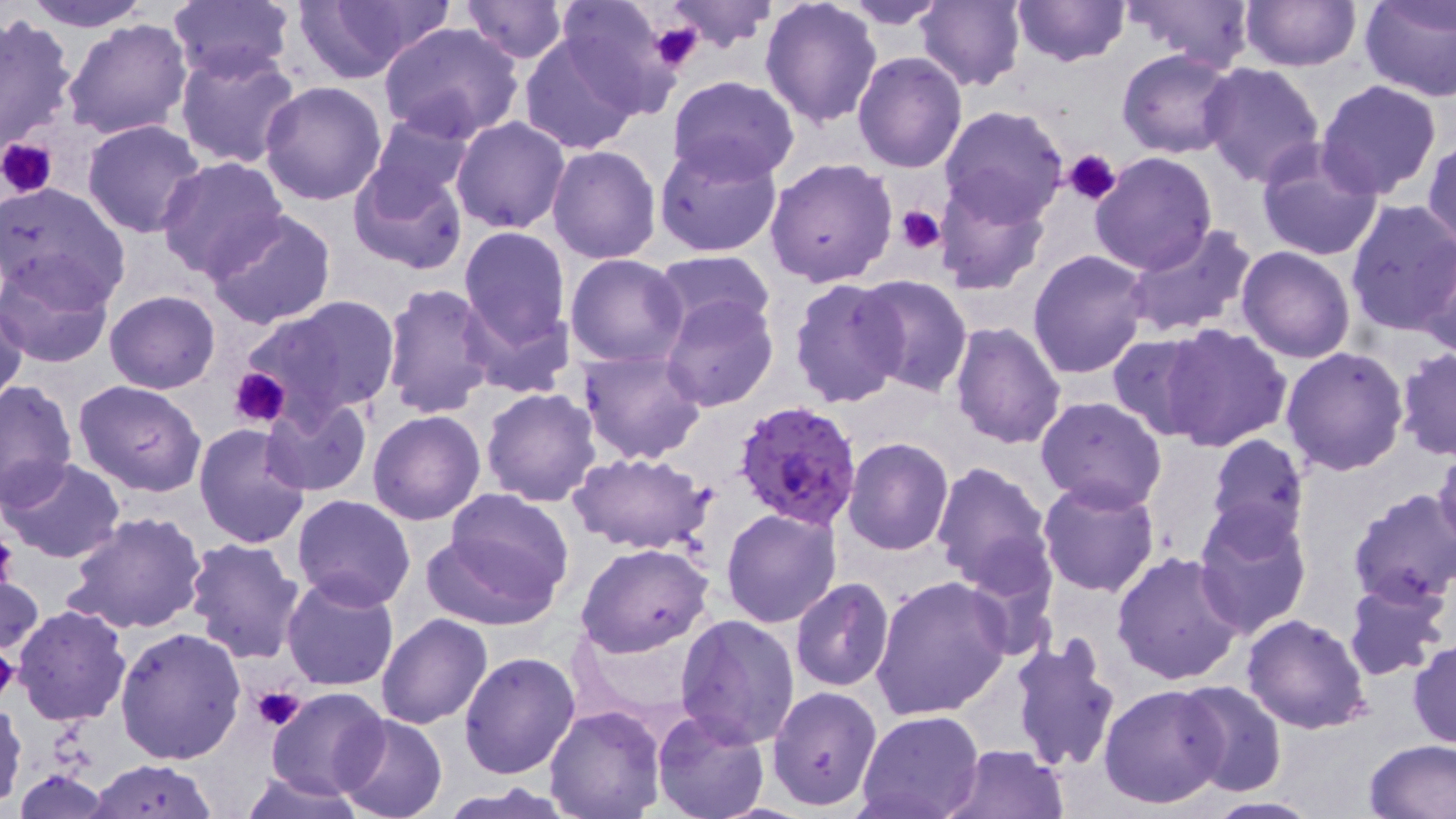
Summary:
  - Coordinate format: approximate bounding boxes as named x1/y1/x2/y2 corners in pixels
  - Platelet locations: (x1=648, y1=18, x2=705, y2=75), (x1=0, y1=136, x2=58, y2=199), (x1=1063, y1=149, x2=1121, y2=205), (x1=894, y1=206, x2=947, y2=253), (x1=229, y1=366, x2=291, y2=429), (x1=0, y1=527, x2=18, y2=595), (x1=0, y1=647, x2=20, y2=704), (x1=252, y1=684, x2=307, y2=733)
  - Plasmodium falciparum-infected red blood cell locations: (x1=732, y1=398, x2=865, y2=532)
  - Uninfected red blood cell locations: (x1=20, y1=0, x2=151, y2=32), (x1=164, y1=0, x2=295, y2=83), (x1=288, y1=0, x2=454, y2=80), (x1=459, y1=0, x2=568, y2=63), (x1=551, y1=0, x2=684, y2=115), (x1=662, y1=0, x2=778, y2=49), (x1=759, y1=0, x2=884, y2=130), (x1=916, y1=0, x2=1027, y2=92), (x1=1008, y1=0, x2=1132, y2=68), (x1=1128, y1=0, x2=1257, y2=69), (x1=1240, y1=0, x2=1360, y2=72), (x1=1359, y1=0, x2=1455, y2=101), (x1=839, y1=1, x2=951, y2=27), (x1=0, y1=12, x2=80, y2=158), (x1=62, y1=18, x2=192, y2=142), (x1=378, y1=21, x2=524, y2=142), (x1=518, y1=33, x2=643, y2=154), (x1=175, y1=45, x2=302, y2=168), (x1=1117, y1=49, x2=1241, y2=158), (x1=852, y1=51, x2=967, y2=172), (x1=1198, y1=62, x2=1325, y2=186), (x1=666, y1=75, x2=801, y2=184), (x1=258, y1=81, x2=388, y2=207), (x1=1316, y1=81, x2=1443, y2=199), (x1=939, y1=104, x2=1068, y2=225), (x1=363, y1=110, x2=477, y2=205), (x1=450, y1=116, x2=570, y2=234), (x1=81, y1=119, x2=208, y2=239), (x1=1426, y1=139, x2=1456, y2=253), (x1=654, y1=140, x2=784, y2=258), (x1=1254, y1=142, x2=1384, y2=263), (x1=546, y1=145, x2=663, y2=264), (x1=1090, y1=152, x2=1218, y2=276), (x1=156, y1=156, x2=290, y2=282), (x1=764, y1=157, x2=898, y2=287), (x1=349, y1=162, x2=469, y2=274), (x1=934, y1=178, x2=1049, y2=299), (x1=0, y1=183, x2=131, y2=311), (x1=1343, y1=201, x2=1456, y2=337), (x1=205, y1=210, x2=339, y2=332), (x1=1123, y1=223, x2=1258, y2=338), (x1=458, y1=227, x2=572, y2=347), (x1=1419, y1=241, x2=1455, y2=361), (x1=1236, y1=246, x2=1355, y2=364), (x1=1026, y1=248, x2=1152, y2=377), (x1=653, y1=250, x2=778, y2=339), (x1=565, y1=254, x2=690, y2=369), (x1=0, y1=261, x2=115, y2=369), (x1=854, y1=275, x2=973, y2=397), (x1=788, y1=276, x2=908, y2=409), (x1=379, y1=282, x2=499, y2=420), (x1=105, y1=290, x2=221, y2=393), (x1=661, y1=293, x2=778, y2=411), (x1=1, y1=295, x2=27, y2=412), (x1=243, y1=296, x2=399, y2=424), (x1=459, y1=297, x2=575, y2=401), (x1=949, y1=322, x2=1067, y2=448), (x1=1159, y1=323, x2=1290, y2=451), (x1=1106, y1=334, x2=1214, y2=440), (x1=1279, y1=346, x2=1409, y2=477), (x1=1395, y1=347, x2=1455, y2=460), (x1=577, y1=349, x2=706, y2=464), (x1=0, y1=380, x2=77, y2=507), (x1=72, y1=381, x2=207, y2=497), (x1=480, y1=387, x2=601, y2=508), (x1=1035, y1=396, x2=1167, y2=512), (x1=261, y1=397, x2=373, y2=497), (x1=368, y1=411, x2=487, y2=526), (x1=193, y1=423, x2=311, y2=549), (x1=1204, y1=433, x2=1308, y2=546), (x1=842, y1=437, x2=954, y2=555), (x1=1433, y1=442, x2=1456, y2=555), (x1=568, y1=451, x2=713, y2=556), (x1=2, y1=456, x2=125, y2=564), (x1=930, y1=460, x2=1054, y2=590), (x1=1037, y1=477, x2=1161, y2=598), (x1=1347, y1=488, x2=1456, y2=607), (x1=292, y1=493, x2=416, y2=610), (x1=429, y1=493, x2=578, y2=627), (x1=1193, y1=506, x2=1314, y2=640), (x1=720, y1=508, x2=844, y2=628), (x1=62, y1=511, x2=207, y2=635), (x1=184, y1=537, x2=305, y2=664), (x1=576, y1=543, x2=715, y2=657), (x1=1111, y1=550, x2=1245, y2=687), (x1=0, y1=570, x2=44, y2=655), (x1=871, y1=575, x2=1013, y2=723), (x1=280, y1=576, x2=399, y2=692), (x1=789, y1=578, x2=895, y2=691), (x1=1342, y1=579, x2=1450, y2=681), (x1=12, y1=605, x2=131, y2=726), (x1=375, y1=613, x2=492, y2=729), (x1=676, y1=613, x2=801, y2=748), (x1=1241, y1=614, x2=1372, y2=734), (x1=114, y1=627, x2=246, y2=764), (x1=1008, y1=633, x2=1122, y2=775), (x1=1409, y1=640, x2=1456, y2=748), (x1=459, y1=651, x2=580, y2=778), (x1=1175, y1=680, x2=1288, y2=799), (x1=1099, y1=683, x2=1229, y2=809), (x1=266, y1=686, x2=390, y2=801), (x1=768, y1=686, x2=882, y2=811), (x1=0, y1=697, x2=26, y2=808), (x1=544, y1=705, x2=667, y2=819), (x1=652, y1=711, x2=772, y2=819), (x1=856, y1=711, x2=984, y2=819), (x1=334, y1=714, x2=448, y2=819), (x1=1363, y1=739, x2=1456, y2=818), (x1=942, y1=743, x2=1070, y2=819), (x1=89, y1=759, x2=219, y2=816), (x1=11, y1=768, x2=118, y2=818), (x1=240, y1=771, x2=366, y2=819), (x1=437, y1=783, x2=576, y2=817), (x1=1198, y1=795, x2=1326, y2=818)
  - Slide-level diagnosis: Plasmodium falciparum
  - Preparation: thin blood film
  - Stain: May-Grünwald-Giemsa
  - Image size: 1456×819 pixels
  - Field of view: single
  - Modality: optical microscopy
  - Magnification: 1000x